Describe the morphology of the erythrocytes.
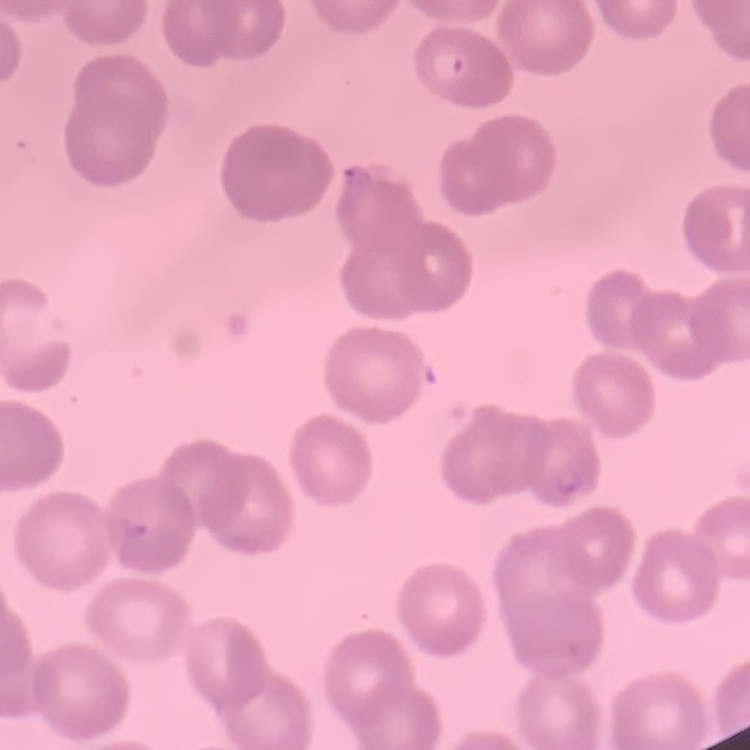

No rouleaux formation.

Thin blood film. One tile cut from a larger photomicrograph. Field's or Giemsa stain.